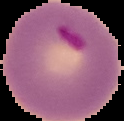 Image is 124×121 pixels. From a thin blood smear. The area outside the segmented cell region is set to black. Malaria status: parasitized.